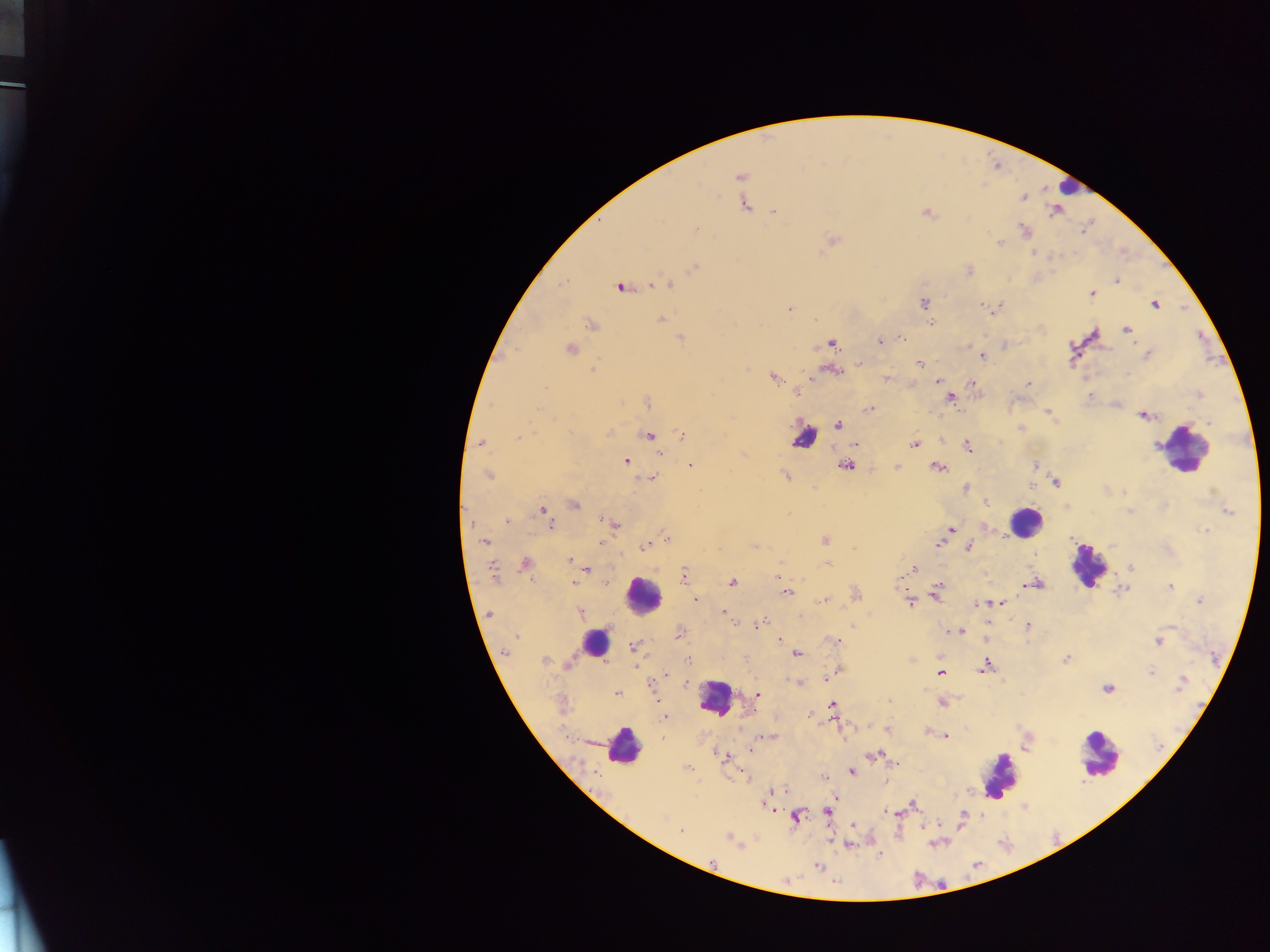

image_size: 1270×952 pixels
malaria_parasite_locations: 'approximate centers as x y in pixels: 740 176; 1023 197; 745 205; 774 212; 926 213; 695 229; 1024 230; 833 240; 1000 242; 1034 252; 694 268; 969 271; 1117 280; 668 286; 621 287; 1092 294; 923 303; 981 304; 1154 304; 789 309; 661 319; 931 323; 590 324; 1126 329; 681 337; 901 339; 881 341; 832 343; 570 349; 1146 354; 983 356; 919 362; 860 363; 594 368; 832 370; 1128 373; 774 378; 887 378; 937 381; 1028 384; 972 385; 545 388; 1089 395; 950 398; 647 403; 870 409; 1048 413; 1144 416; 1209 422; 838 424; 608 433; 683 435; 649 436; 518 437; 481 443; 855 444; 914 444; 968 445; 661 454; 625 461; 1034 464; 690 465; 845 466; 896 467; 938 467; 488 475; 785 476; 652 478; 1056 481; 966 489; 986 503; 574 505; 543 510; 1227 511; 602 519; 506 521; 471 523; 551 523; 615 524; 950 529; 1205 531; 666 538; 825 540; 484 542; 601 543; 938 544; 645 545; 968 547; 569 560; 525 564; 828 565; 1130 567; 587 569; 912 569; 492 572; 684 575; 778 576; 605 582; 732 582; 575 583; 1034 583; 1170 587; 1122 589; 786 592; 935 593; 856 595; 696 600; 824 601; 909 602; 1001 602; 1199 602; 979 603; 991 603; 723 612; 580 613; 490 614; 760 624; 1027 626; 952 631; 959 632; 679 633; 517 636; 780 638; 985 638; 836 641; 1158 641; 633 646; 505 652; 797 655; 1066 659; 544 660; 688 660; 637 667; 985 667; 838 670; 1151 672; 940 673; 666 675; 798 683; 1182 684; 1108 688; 617 694; 758 694; 889 700; 942 702; 832 705; 665 717; 927 732; 946 736; 769 737; 750 750; 873 755; 725 757; 894 763; 687 768; 851 771; 823 778; 777 790; 772 793; 914 805; 766 806; 889 812; 828 813; 963 816; 796 817; 663 818; 853 826; 924 827; 681 832; 729 839; 818 866'
preparation: thick blood smear
leukocyte_locations: 'approximate centers as x y in pixels: 1068 188; 804 438; 1184 450; 1025 522; 1088 565; 643 594; 594 642; 715 697; 623 746; 1099 755; 998 773'
capture: mobile-phone photograph through a microscope
field_of_view: single
country: Ghana